Describe the morphology of the erythrocytes.
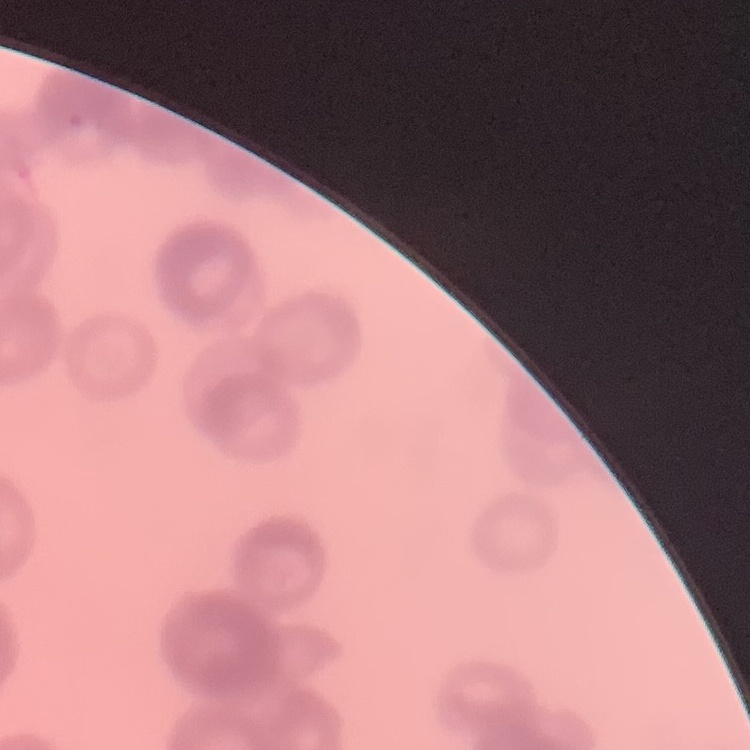

They show rouleaux formation.

Summary:
  - Stain: Field's or Giemsa
  - Image type: square crop of a larger photomicrograph
  - Preparation: thin blood film